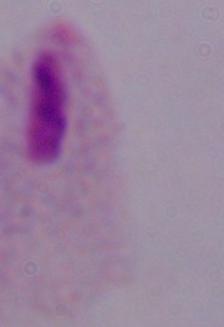

identification = trichomonad
magnification = 1000x
modality = photomicrograph